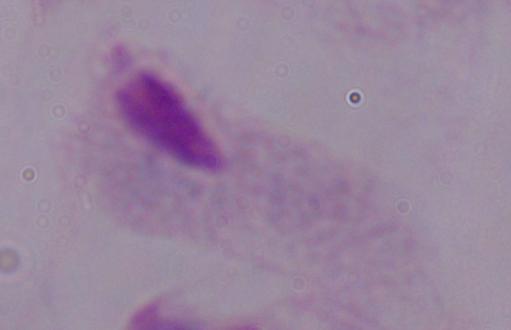
Photomicrograph. A trichomonad is seen. Captured at 1000x magnification.